Assess this cell for malaria.
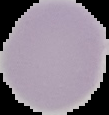

It is uninfected.

Image is 109×115 pixels. From a thin blood film. Cell region segmented out of the field of view; the surrounding area is masked to black.